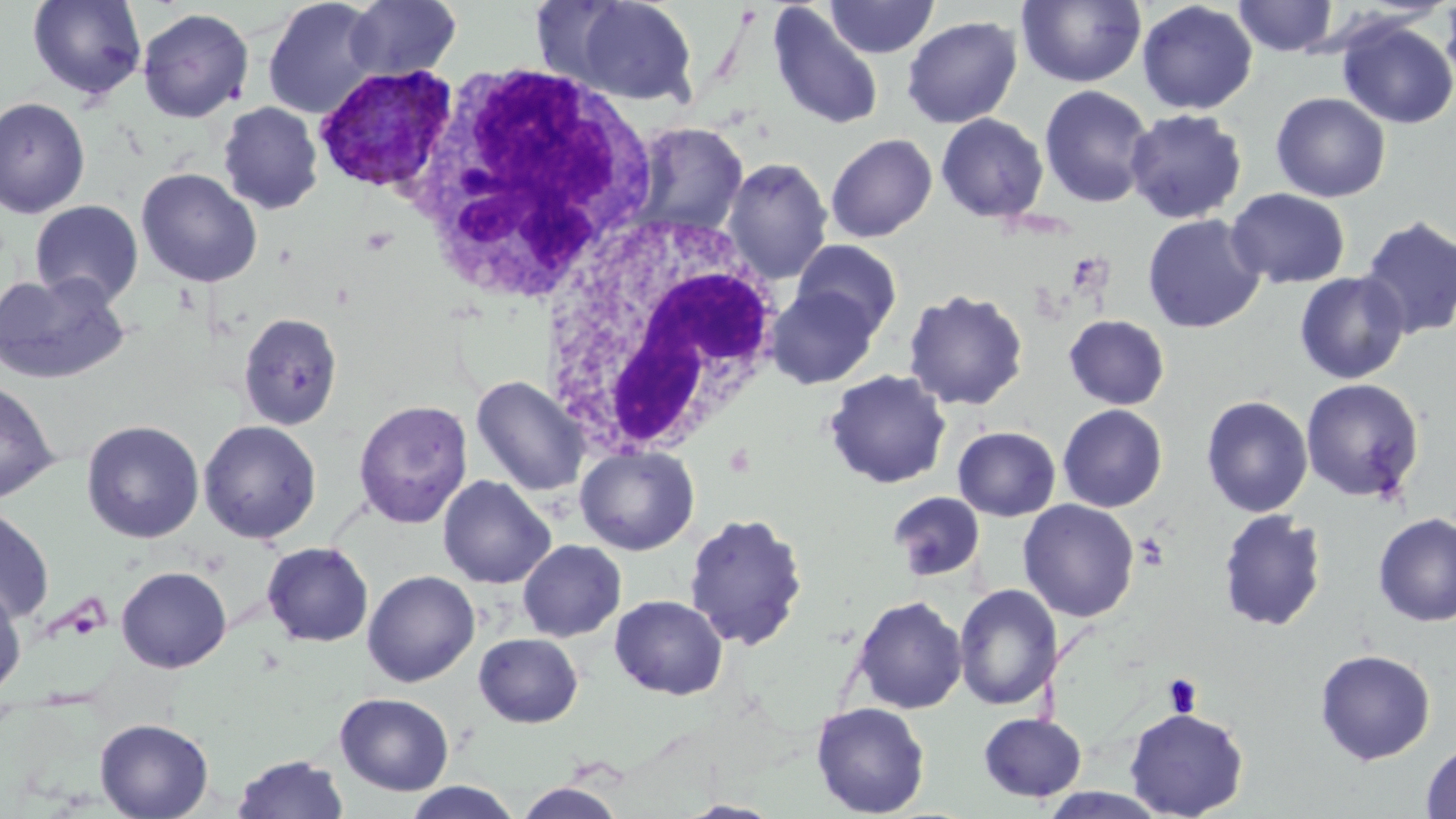
Summary:
  - Coordinate format: approximate bounding boxes as (x1,y1)-(x2,y2) corner pairs in pixels
  - White blood cell locations (subset): (540,209)-(785,460)
  - Plasmodium vivax-infected red blood cell locations: (312,65)-(459,196)
  - Platelet locations: (1134,532)-(1169,571), (1163,674)-(1203,717)
  - Uninfected red blood cell locations (subset): (27,0)-(146,101), (263,0)-(383,119), (344,0)-(462,82), (558,0)-(702,106), (825,0)-(939,59), (1016,0)-(1146,87), (1232,0)-(1338,57), (1136,1)-(1258,115), (1440,1)-(1456,95), (766,4)-(884,131), (137,8)-(254,123), (901,15)-(1022,128), (1336,18)-(1456,129), (1039,85)-(1155,209), (1271,92)-(1391,202), (0,96)-(90,218), (216,102)-(323,215), (1124,108)-(1248,224), (936,113)-(1049,223), (626,122)-(749,242), (825,133)-(937,242), (722,157)-(833,285), (136,168)-(263,287), (1226,188)-(1351,289), (30,200)-(145,306), (1142,214)-(1267,333), (1358,216)-(1456,340), (792,240)-(903,336), (1294,270)-(1411,384), (0,272)-(131,385), (765,285)-(882,389), (903,288)-(1029,410), (239,312)-(343,430), (1063,314)-(1170,410), (824,369)-(952,489), (471,375)-(590,496), (1300,378)-(1425,503), (0,379)-(59,503), (1201,395)-(1313,517), (353,400)-(473,529), (1057,404)-(1168,512), (81,420)-(204,543), (198,420)-(322,544), (952,426)-(1061,521), (575,445)-(699,556), (437,475)-(556,589), (888,491)-(985,581), (1018,499)-(1140,622), (0,506)-(54,624), (1216,508)-(1328,632), (683,511)-(808,651), (1373,512)-(1456,626), (517,540)-(626,642), (262,541)-(373,647), (116,566)-(232,673), (362,570)-(480,687), (0,582)-(26,698), (953,583)-(1064,711), (610,594)-(728,700), (851,595)-(967,714), (474,632)-(583,727), (1315,648)-(1436,764), (335,692)-(454,796), (810,702)-(930,817), (1124,707)-(1249,819), (978,712)-(1088,802), (94,718)-(214,819), (1420,741)-(1456,819), (232,754)-(348,818), (402,781)-(524,818), (514,781)-(626,819), (1039,788)-(1172,819), (678,800)-(784,818)
  - Slide-level diagnosis: Plasmodium vivax
  - Stain: May-Grünwald-Giemsa
  - Image size: 1456×819 pixels
  - Preparation: thin blood film
  - Field of view: one of a larger specimen
  - Magnification: 1000x
  - Modality: light microscopy